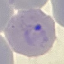

{
  "malaria_status": "parasitized",
  "stain": "Giemsa",
  "image_type": "cell patch, automatically extracted from a larger field of view and resized to 64 × 64 pixels",
  "capture": "smartphone through the microscope eyepiece",
  "preparation": "thin smear"
}